Report the malaria status of this cell.
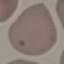

Uninfected.

capture = smartphone through the microscope eyepiece
stain = Giemsa
image type = cell patch, automatically extracted from a larger field of view and resized to 64 × 64 pixels
preparation = thin blood smear